Name the cell type shown.
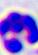

A leukocyte.

magnification: 400x
modality: photomicrograph